Classify this cell by malaria status.
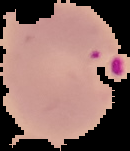
It is parasitized.

{
  "image_size": "130×151 pixels",
  "image_type": "segmented cell region on a black background",
  "preparation": "thin blood smear"
}